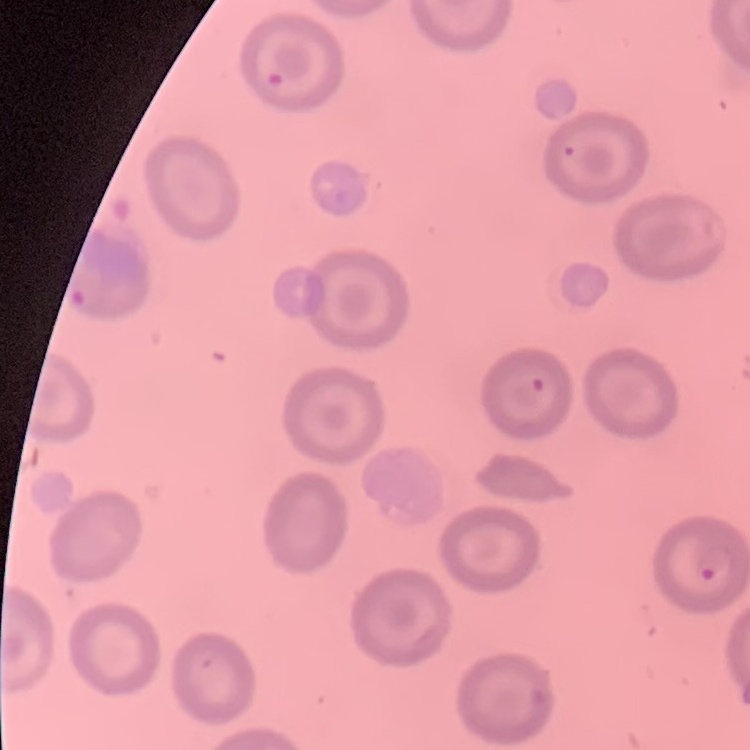

Summary:
  - Red blood cell morphology: no rouleaux formation
  - Preparation: thin blood smear
  - Stain: Field's or Giemsa
  - Image type: square crop of a larger photomicrograph